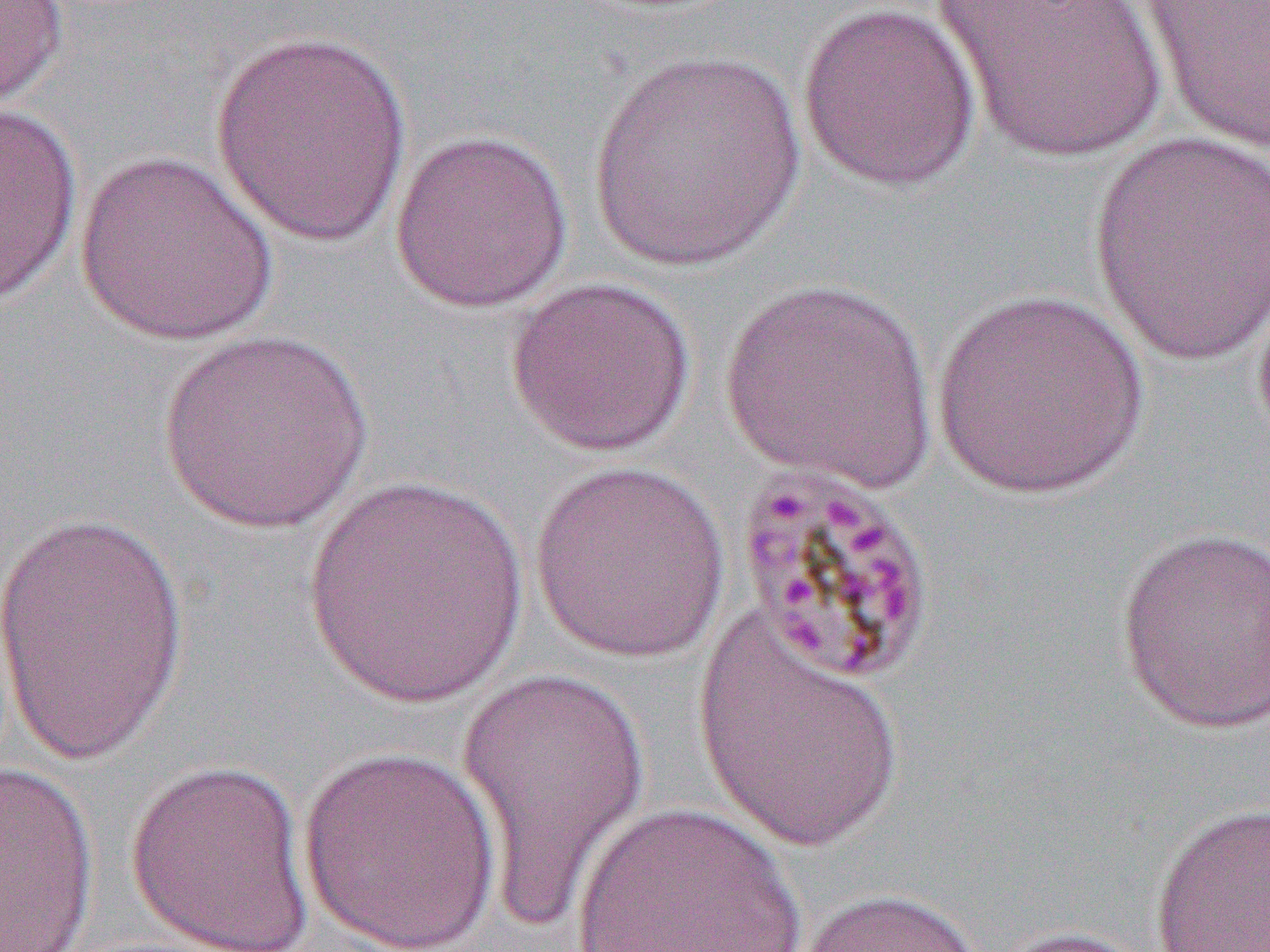

slide_level_diagnosis: Plasmodium malariae
modality: light microscopy
field_of_view: one of a larger specimen
magnification: 1000x
uninfected_red_blood_cell_locations: 'approximate bounding boxes as (x1,y1)-(x2,y2) corner pairs in pixels: (796,0)-(983,193), (932,0)-(1169,165), (0,1)-(70,116), (1132,1)-(1270,154), (207,30)-(415,248), (590,49)-(806,273), (0,101)-(84,306), (388,128)-(573,314), (1088,129)-(1270,369), (74,151)-(281,347), (504,275)-(697,457), (721,275)-(938,494), (930,289)-(1151,499), (157,329)-(374,535), (527,461)-(732,665), (304,471)-(528,709), (0,503)-(195,775), (1114,525)-(1270,735), (691,606)-(907,852), (451,662)-(653,931), (296,747)-(504,952), (124,757)-(316,951), (0,760)-(101,951), (568,800)-(806,951), (1149,801)-(1270,951), (788,887)-(992,952), (978,924)-(1158,952)'
image_size: 1270×952 pixels
preparation: thin blood smear